Identify the blood parasite species.
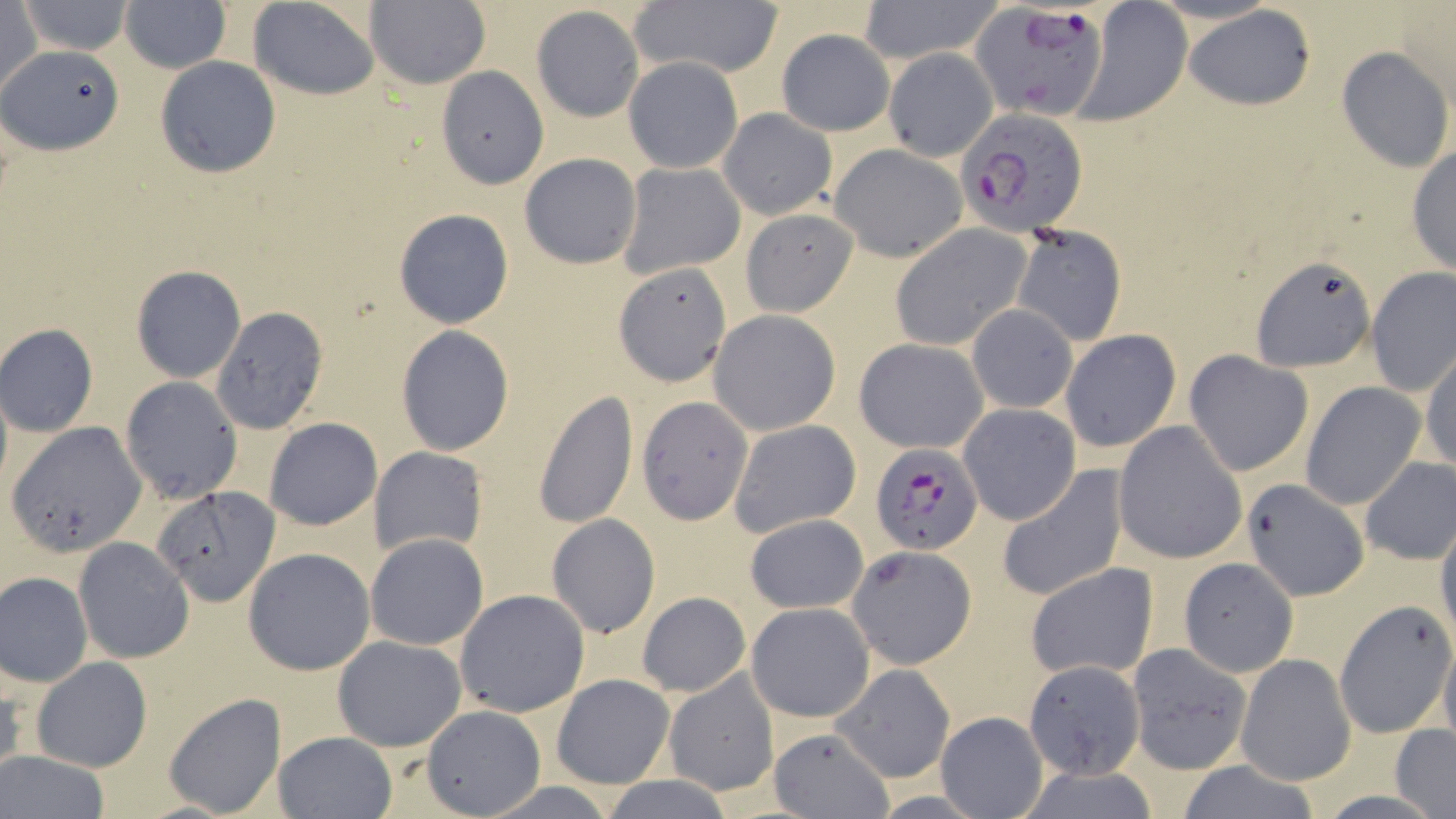
Plasmodium falciparum.

Summary:
  - Coordinate format: approximate bounding boxes as [x1, y1, x2, y2] in pixels
  - Plasmodium falciparum-infected red blood cell locations: [973, 2, 1109, 121], [954, 107, 1089, 240], [870, 443, 985, 557]
  - Uninfected red blood cell locations: [248, 0, 381, 99], [864, 0, 991, 66], [19, 1, 133, 55], [0, 2, 44, 100], [121, 2, 230, 73], [363, 2, 490, 89], [631, 2, 782, 81], [1078, 4, 1190, 121], [1184, 5, 1317, 112], [532, 7, 644, 123], [777, 28, 895, 136], [4, 44, 123, 154], [1337, 46, 1453, 173], [883, 49, 997, 161], [154, 56, 282, 177], [624, 57, 744, 172], [435, 65, 546, 187], [718, 108, 837, 219], [830, 144, 967, 261], [1406, 146, 1455, 274], [519, 153, 642, 270], [617, 161, 745, 279], [740, 207, 858, 318], [394, 208, 514, 327], [889, 225, 1031, 351], [1011, 225, 1126, 346], [1251, 255, 1376, 371], [614, 263, 733, 386], [131, 266, 245, 383], [1366, 268, 1456, 396], [209, 305, 330, 432], [967, 305, 1077, 414], [709, 310, 840, 435], [0, 323, 99, 436], [396, 326, 515, 456], [1059, 330, 1180, 453], [853, 338, 987, 454], [1421, 348, 1456, 474], [1184, 350, 1314, 475], [120, 377, 242, 503], [1303, 384, 1426, 509], [531, 389, 639, 528], [637, 397, 754, 523], [957, 404, 1080, 525], [263, 418, 381, 531], [7, 419, 148, 556], [728, 419, 861, 539], [1114, 420, 1247, 562], [371, 447, 486, 557], [1358, 456, 1456, 564], [996, 465, 1128, 603], [1241, 479, 1372, 603], [153, 486, 281, 606], [743, 513, 870, 614], [547, 514, 660, 639], [1435, 520, 1456, 646], [366, 533, 489, 651], [73, 537, 194, 663], [846, 545, 978, 669], [243, 548, 375, 676], [1179, 558, 1298, 677], [1025, 562, 1158, 681], [1, 571, 93, 685], [453, 589, 589, 718], [634, 593, 751, 698], [1334, 600, 1455, 739], [746, 602, 874, 721], [332, 635, 467, 752], [1438, 636, 1456, 750], [1126, 642, 1251, 774], [1236, 654, 1356, 785], [30, 656, 152, 772], [1028, 659, 1149, 782], [0, 664, 25, 780], [832, 665, 954, 783], [664, 670, 780, 796], [551, 673, 674, 789], [162, 691, 287, 816], [420, 705, 546, 817], [937, 709, 1048, 818], [768, 726, 894, 818], [1392, 726, 1456, 815], [272, 730, 398, 819], [0, 751, 110, 819], [1171, 760, 1325, 818], [598, 777, 737, 817]
  - Magnification: 1000x
  - Stain: May-Grünwald-Giemsa
  - Modality: optical microscopy
  - Preparation: thin blood film
  - Image size: 1456×819 pixels
  - Field of view: single